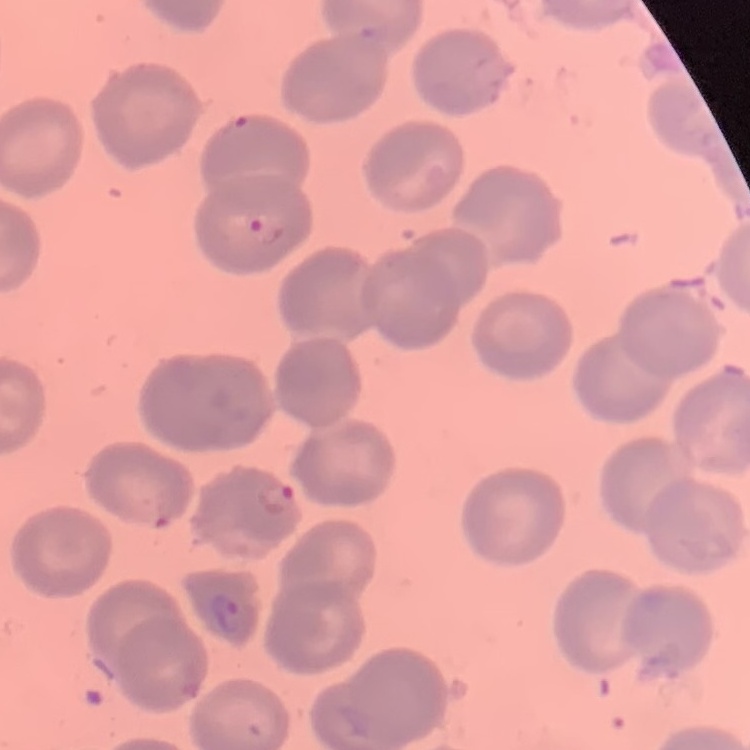
erythrocyte morphology = no rouleaux formation
preparation = thin blood film
image type = square crop of a larger photomicrograph
stain = Field's or Giemsa